Identify the blood parasite species.
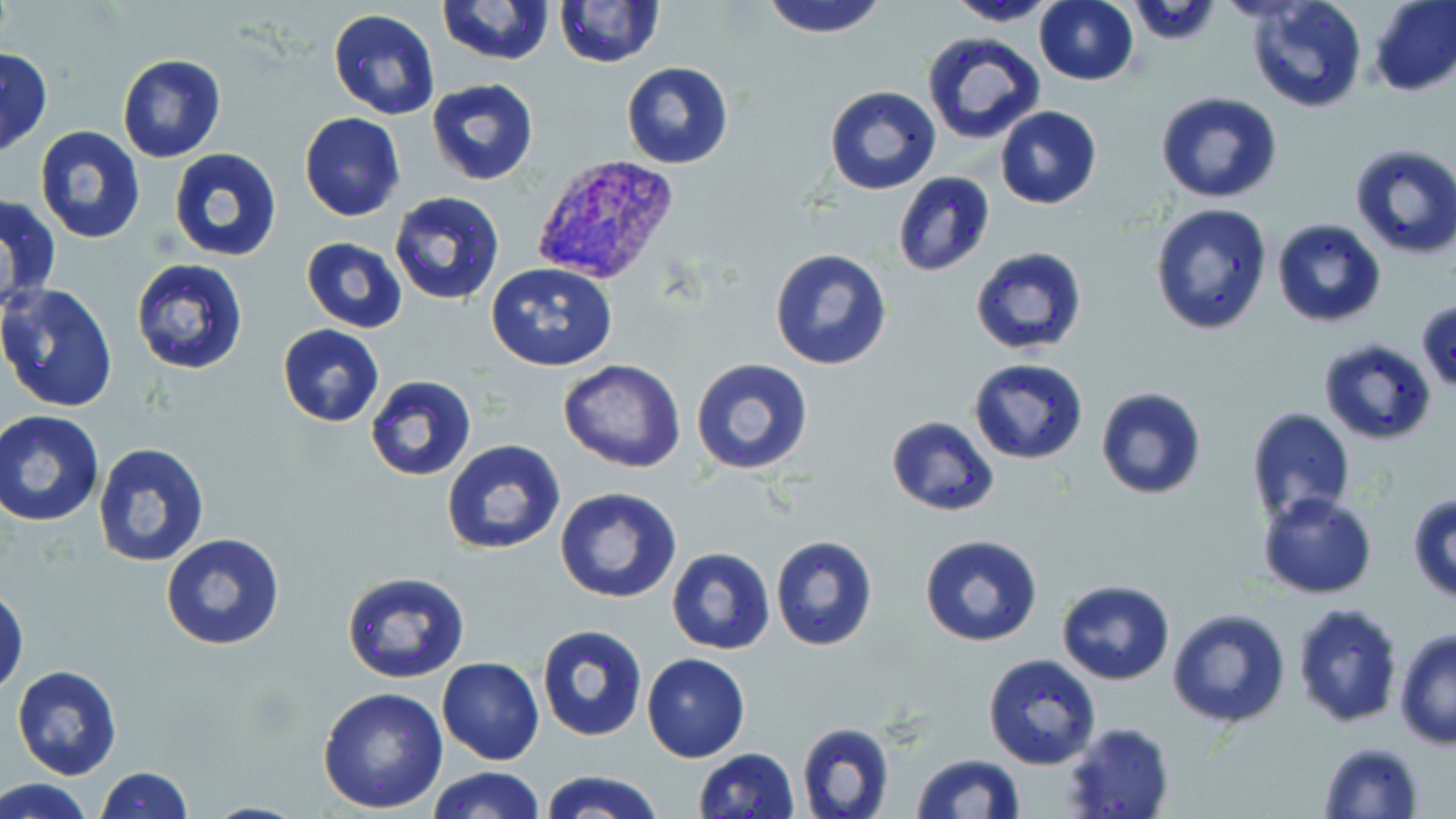

Plasmodium vivax.

Approximate bounding boxes as named x1/y1/x2/y2 corners in pixels. Uninfected red blood cell locations: (x1=436, y1=0, x2=556, y2=67), (x1=761, y1=0, x2=888, y2=40), (x1=1034, y1=0, x2=1138, y2=85), (x1=1243, y1=0, x2=1368, y2=114), (x1=1370, y1=0, x2=1456, y2=96), (x1=555, y1=1, x2=665, y2=68), (x1=947, y1=1, x2=1064, y2=26), (x1=328, y1=8, x2=440, y2=121), (x1=921, y1=32, x2=1047, y2=148), (x1=1, y1=47, x2=52, y2=160), (x1=116, y1=53, x2=226, y2=163), (x1=621, y1=62, x2=734, y2=169), (x1=424, y1=79, x2=540, y2=186), (x1=824, y1=87, x2=941, y2=194), (x1=1156, y1=91, x2=1283, y2=204), (x1=995, y1=106, x2=1102, y2=210), (x1=299, y1=112, x2=405, y2=221), (x1=34, y1=124, x2=149, y2=245), (x1=1348, y1=144, x2=1456, y2=261), (x1=168, y1=148, x2=282, y2=261), (x1=893, y1=172, x2=995, y2=277), (x1=388, y1=192, x2=506, y2=307), (x1=1, y1=193, x2=62, y2=315), (x1=1150, y1=204, x2=1274, y2=335), (x1=1272, y1=218, x2=1388, y2=328), (x1=301, y1=238, x2=409, y2=333), (x1=970, y1=246, x2=1089, y2=357), (x1=769, y1=248, x2=893, y2=371), (x1=131, y1=258, x2=249, y2=374), (x1=487, y1=263, x2=618, y2=370), (x1=0, y1=283, x2=119, y2=414), (x1=1416, y1=299, x2=1456, y2=392), (x1=277, y1=325, x2=383, y2=427), (x1=1318, y1=339, x2=1437, y2=445), (x1=558, y1=358, x2=687, y2=473), (x1=968, y1=358, x2=1090, y2=465), (x1=691, y1=359, x2=815, y2=476), (x1=365, y1=375, x2=476, y2=482), (x1=1095, y1=387, x2=1207, y2=499), (x1=1244, y1=408, x2=1357, y2=525), (x1=0, y1=411, x2=103, y2=527), (x1=885, y1=415, x2=1001, y2=516), (x1=441, y1=439, x2=566, y2=555), (x1=93, y1=442, x2=211, y2=569), (x1=554, y1=486, x2=682, y2=603), (x1=1257, y1=491, x2=1378, y2=599), (x1=1407, y1=491, x2=1456, y2=602), (x1=160, y1=532, x2=285, y2=652), (x1=919, y1=533, x2=1044, y2=647), (x1=769, y1=535, x2=879, y2=653), (x1=666, y1=546, x2=776, y2=655), (x1=341, y1=571, x2=471, y2=684), (x1=1056, y1=578, x2=1174, y2=686), (x1=1, y1=587, x2=27, y2=695), (x1=1293, y1=602, x2=1405, y2=728), (x1=1167, y1=608, x2=1292, y2=730), (x1=535, y1=624, x2=648, y2=743), (x1=1394, y1=630, x2=1455, y2=750), (x1=642, y1=653, x2=750, y2=762), (x1=982, y1=653, x2=1103, y2=770), (x1=437, y1=657, x2=544, y2=765), (x1=11, y1=665, x2=123, y2=780), (x1=318, y1=686, x2=449, y2=813), (x1=796, y1=720, x2=895, y2=819), (x1=1062, y1=722, x2=1175, y2=819), (x1=1318, y1=741, x2=1425, y2=818), (x1=692, y1=747, x2=801, y2=819), (x1=910, y1=752, x2=1025, y2=819), (x1=424, y1=765, x2=544, y2=819), (x1=97, y1=766, x2=193, y2=819), (x1=540, y1=769, x2=662, y2=819), (x1=2, y1=778, x2=91, y2=818). Plasmodium vivax-infected red blood cell locations: (x1=530, y1=154, x2=680, y2=287). Optical microscopy. Single field of view. Thin blood film. May-Grünwald-Giemsa-stained preparation. Captured at 1000x magnification. Image is 1456×819 pixels.